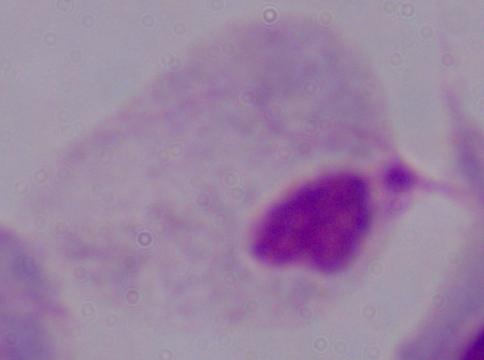
1000x magnification. A trichomonad is shown. Micrograph.